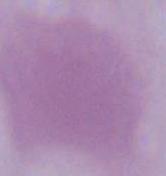
Summary:
  - Modality: micrograph
  - Magnification: 1000x
  - Identification: erythrocyte